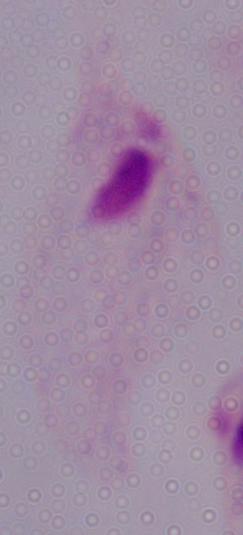
Captured at 1000x magnification. A trichomonad is shown. Photomicrograph.